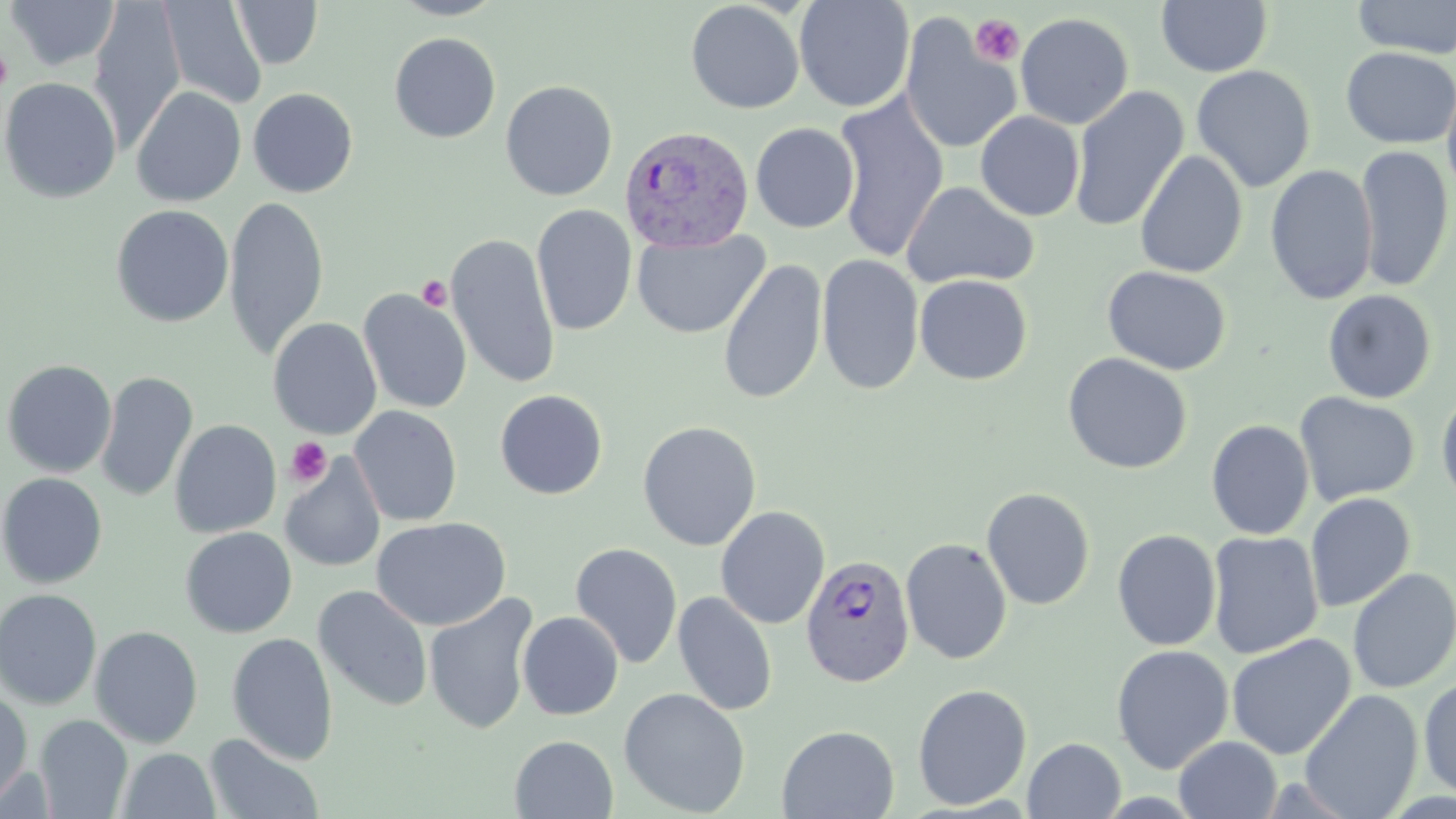

Summary:
  - Coordinate format: approximate bounding boxes as (x1,y1)-(x2,y2) corner pairs in pixels
  - Platelet locations: (970,14)-(1025,67), (1,47)-(14,92), (417,276)-(453,311), (285,437)-(333,486)
  - Plasmodium vivax-infected red blood cell locations: (619,124)-(754,253), (800,553)-(916,687)
  - Uninfected red blood cell locations: (5,0)-(119,72), (794,0)-(915,113), (1352,0)-(1456,59), (88,1)-(186,150), (158,1)-(267,110), (231,1)-(323,69), (685,1)-(805,114), (1156,1)-(1273,77), (1015,12)-(1134,130), (900,14)-(1021,156), (389,32)-(501,143), (1340,47)-(1456,149), (1191,64)-(1316,193), (1441,73)-(1456,204), (0,76)-(122,204), (500,80)-(618,201), (131,85)-(246,207), (1068,85)-(1189,234), (247,88)-(358,197), (832,93)-(949,262), (975,111)-(1085,221), (750,122)-(860,233), (1355,144)-(1454,292), (1134,149)-(1248,279), (1265,164)-(1379,305), (902,181)-(1040,290), (224,195)-(330,358), (531,204)-(637,336), (111,205)-(234,327), (632,229)-(770,339), (445,232)-(560,389), (816,254)-(924,395), (717,258)-(828,405), (1102,265)-(1231,375), (914,274)-(1033,385), (358,288)-(472,414), (1322,289)-(1437,404), (268,317)-(382,439), (1062,352)-(1192,474), (2,359)-(117,478), (96,371)-(198,503), (1436,385)-(1456,512), (494,389)-(608,500), (1294,392)-(1420,506), (349,405)-(462,526), (169,419)-(281,538), (637,420)-(762,551), (1206,420)-(1314,540), (280,453)-(386,573), (0,472)-(107,589), (981,487)-(1095,610), (1305,492)-(1416,613), (716,505)-(830,629), (371,517)-(511,631), (180,527)-(298,638), (1112,529)-(1222,651), (1206,531)-(1324,659), (900,538)-(1013,665), (569,542)-(683,669), (1346,567)-(1456,695), (312,584)-(433,711), (0,588)-(103,710), (672,591)-(778,717), (424,593)-(539,735), (517,611)-(624,720), (90,625)-(203,748), (227,632)-(339,764), (1227,633)-(1356,760), (1110,644)-(1234,774), (1418,675)-(1456,800), (912,683)-(1032,811), (619,687)-(751,817), (0,689)-(32,810), (1299,689)-(1423,819), (34,714)-(133,818), (776,724)-(900,818), (204,734)-(324,818), (509,735)-(618,818), (1173,736)-(1282,819), (1023,737)-(1125,818), (116,748)-(220,819)
  - Slide-level diagnosis: Plasmodium vivax
  - Stain: May-Grünwald-Giemsa
  - Modality: optical microscopy
  - Preparation: thin blood smear
  - Field of view: one of a larger specimen
  - Image size: 1456×819 pixels
  - Magnification: 1000x